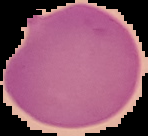 Image is 148×136 pixels. From a thin blood smear. Malaria status: parasitized. Cell region segmented out of the field of view; the surrounding area is masked to black.